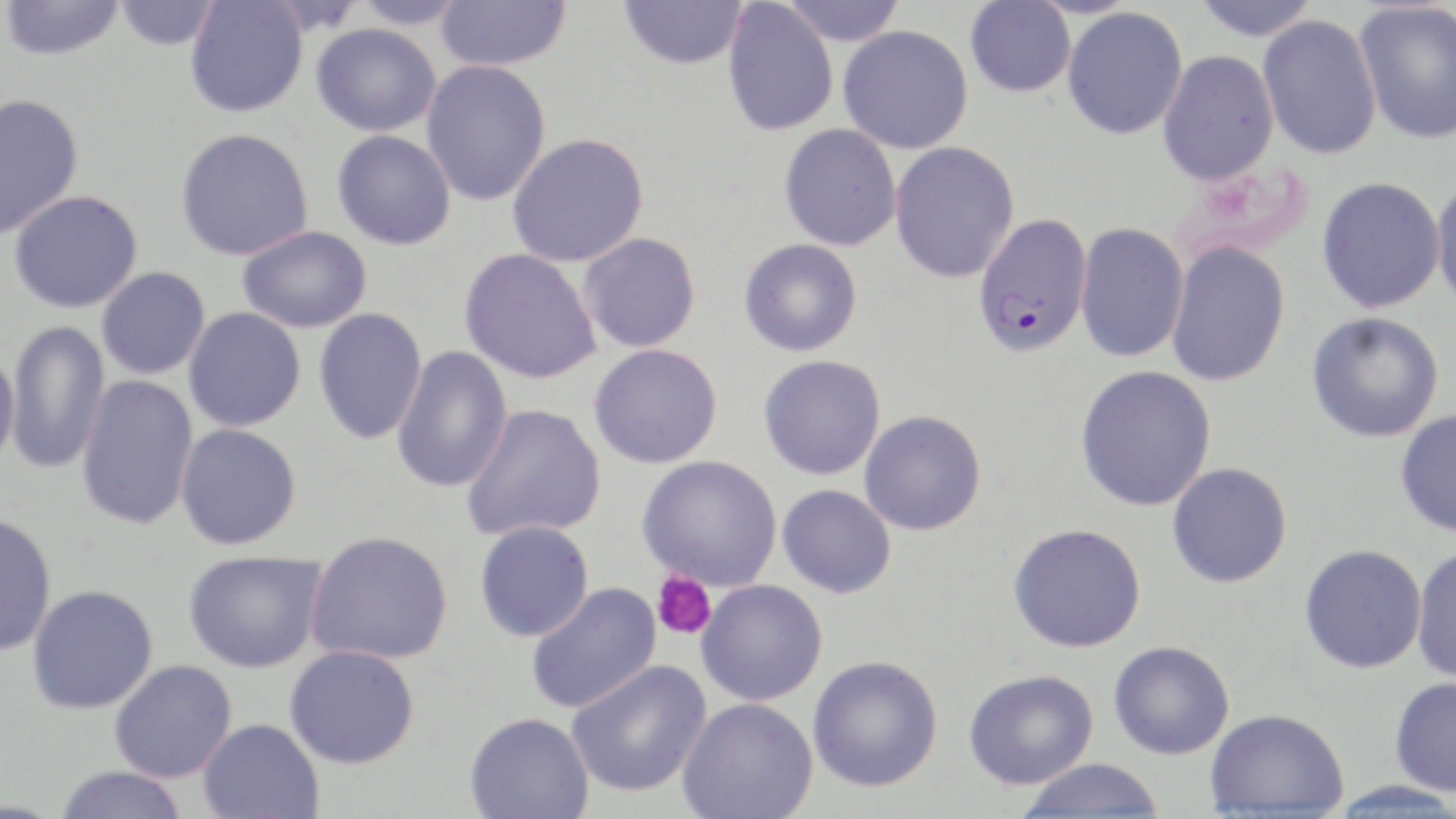

{
  "slide_level_diagnosis": "Plasmodium falciparum",
  "preparation": "thin blood smear",
  "platelet_locations": "approximate bounding boxes as (x1,y1)-(x2,y2) corner pairs in pixels: (652,570)-(717,640)",
  "plasmodium_falciparum_infected_red_blood_cell_locations": "approximate bounding boxes as (x1,y1)-(x2,y2) corner pairs in pixels: (971,212)-(1094,360)",
  "modality": "optical microscopy",
  "magnification": "1000x",
  "stain": "May-Grünwald-Giemsa",
  "image_size": "1456×819 pixels",
  "uninfected_red_blood_cell_locations": "approximate bounding boxes as (x1,y1)-(x2,y2) corner pairs in pixels: (0,0)-(127,62), (112,0)-(222,50), (184,0)-(308,118), (350,0)-(470,29), (435,0)-(571,71), (619,0)-(748,70), (778,0)-(907,46), (964,0)-(1076,98), (1191,0)-(1319,41), (722,1)-(838,136), (1354,1)-(1456,145), (1061,6)-(1188,140), (1257,13)-(1382,160), (311,23)-(441,136), (838,25)-(973,154), (1157,50)-(1279,186), (421,60)-(550,206), (0,93)-(84,241), (778,124)-(902,251), (174,128)-(314,262), (332,130)-(456,250), (506,133)-(649,268), (889,141)-(1020,284), (1431,175)-(1456,313), (1316,176)-(1446,314), (8,190)-(144,313), (1075,222)-(1189,363), (236,226)-(372,333), (578,232)-(701,353), (739,238)-(862,357), (1166,241)-(1291,387), (459,248)-(602,384), (96,267)-(210,380), (183,307)-(306,432), (314,307)-(427,445), (1307,312)-(1445,442), (6,320)-(111,475), (589,343)-(723,468), (391,345)-(513,493), (0,348)-(20,471), (758,355)-(886,480), (1075,365)-(1217,512), (76,374)-(199,530), (461,404)-(607,541), (1395,409)-(1456,538), (859,410)-(987,536), (176,423)-(302,550), (637,455)-(782,590), (1167,462)-(1293,588), (777,484)-(897,598), (0,512)-(57,657), (474,520)-(594,642), (1008,523)-(1147,653), (306,531)-(454,665), (1299,544)-(1427,673), (1412,544)-(1456,683), (184,550)-(327,673), (696,580)-(828,706), (526,582)-(663,714), (27,584)-(158,714), (1109,641)-(1234,759), (285,645)-(420,769), (808,656)-(943,794), (109,659)-(237,783), (567,659)-(713,799), (964,670)-(1098,790), (1389,677)-(1456,797), (677,698)-(819,819), (1204,708)-(1349,816), (464,713)-(594,819), (197,718)-(324,818), (1018,758)-(1165,817), (54,765)-(188,819), (1328,781)-(1456,817)",
  "field_of_view": "one of a larger specimen"
}